Assess the morphology of the red blood cells.
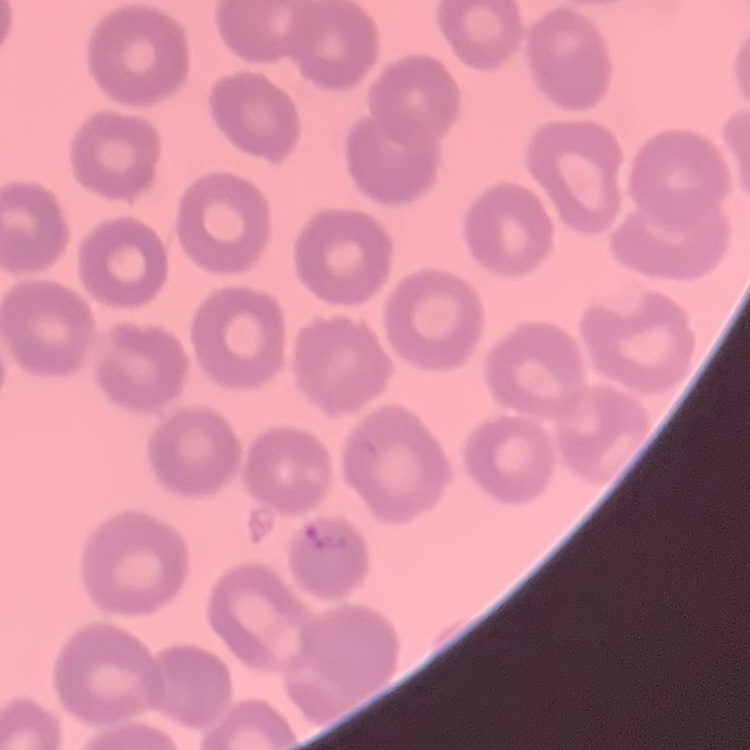
No rouleaux formation.

Summary:
  - Preparation: thin blood film
  - Image type: one tile cut from a larger photomicrograph
  - Stain: Field's or Giemsa